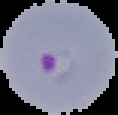 From a thin blood film. Image is 118×115 pixels. Segmented cell region on a black background. Malaria status: parasitized.